Classify this cell by malaria status.
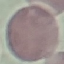

Uninfected.

Automatically extracted cell patch, resized to 64 × 64 pixels. Photographed with a smartphone camera at the microscope eyepiece. Thin smear of blood. Giemsa stain.